Describe the morphology of the erythrocytes.
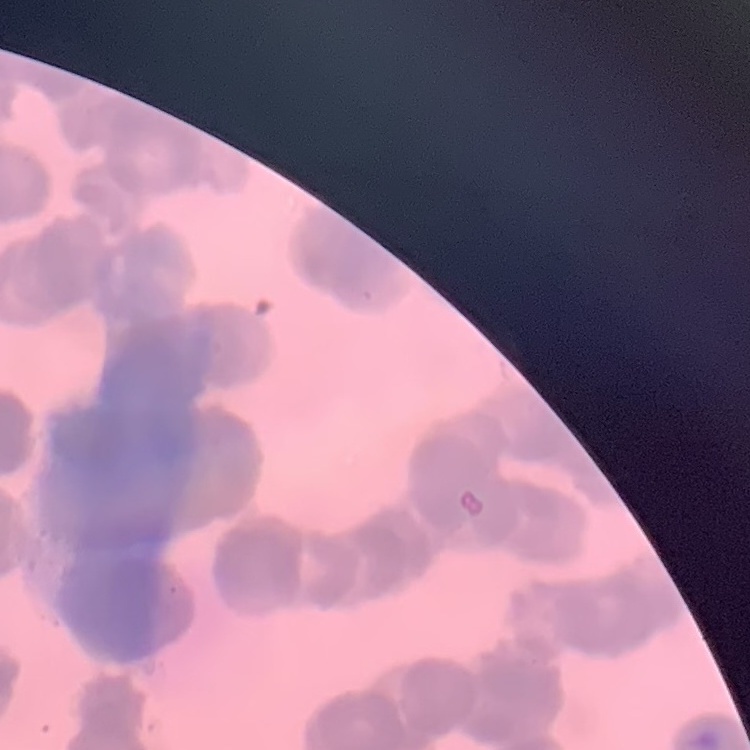

Rouleaux formation.

Thin blood film. Square crop of a larger photomicrograph. Stained with either Field's or Giemsa.